Identify the parasite.
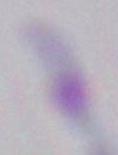

This is Toxoplasma gondii.

Captured at 1000x magnification. Photomicrograph.